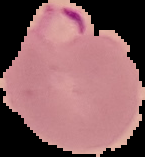

Summary:
  - Image size: 145×157 pixels
  - Image type: segmented cell region on a black background
  - Preparation: thin blood smear
  - Result: Plasmodium parasites detected